State which parasite is depicted.
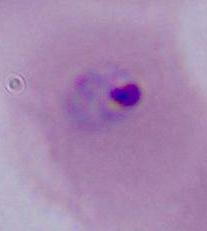
Plasmodium.

{
  "modality": "micrograph",
  "magnification": "400x or 1000x"
}